Locate every blood parasite and identify its species.
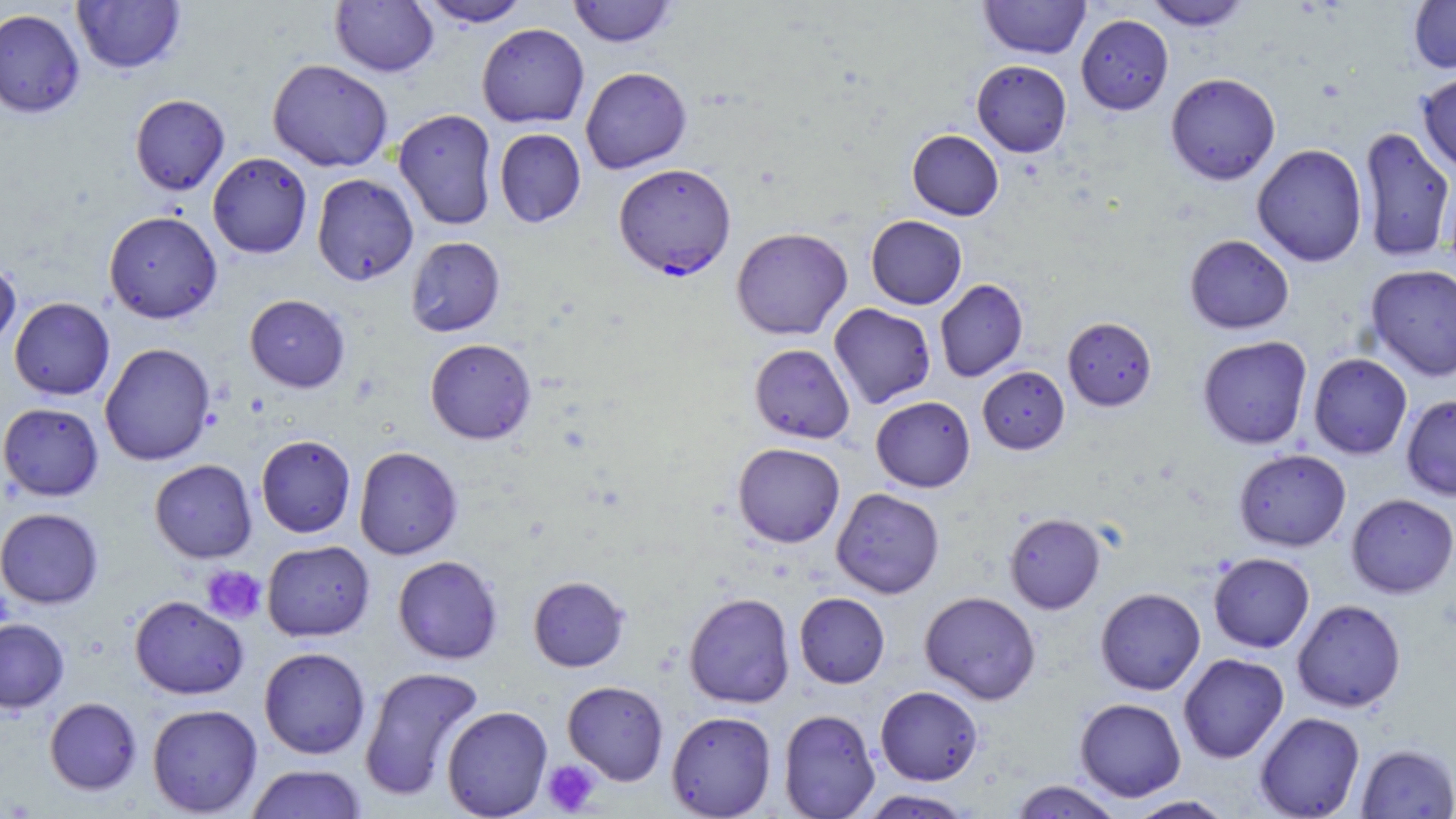

Approximate bounding boxes as [x1, y1, x2, y2] in pixels.
Plasmodium falciparum-infected red blood cells: [613, 164, 737, 280].
No Plasmodium ovale, Plasmodium malariae, Plasmodium vivax, Babesia divergens, or Trypanosoma brucei observed.

Summary:
  - Uninfected red blood cell locations: [71, 0, 186, 74], [330, 0, 438, 77], [417, 0, 532, 27], [567, 0, 678, 47], [979, 0, 1090, 59], [1143, 0, 1253, 31], [1408, 0, 1456, 73], [0, 8, 85, 118], [1076, 14, 1174, 114], [476, 23, 590, 128], [267, 59, 393, 172], [971, 60, 1072, 157], [580, 67, 691, 174], [1417, 71, 1456, 175], [1165, 72, 1281, 185], [130, 94, 230, 195], [393, 109, 498, 231], [1357, 126, 1455, 262], [494, 128, 586, 228], [907, 129, 1004, 220], [1252, 143, 1368, 267], [207, 152, 312, 259], [311, 174, 419, 285], [103, 211, 222, 323], [866, 215, 967, 309], [731, 227, 853, 340], [1184, 234, 1294, 334], [405, 236, 505, 337], [0, 258, 21, 352], [1365, 264, 1456, 381], [935, 279, 1028, 382], [245, 294, 350, 392], [9, 297, 115, 400], [828, 303, 936, 409], [1062, 316, 1157, 411], [1197, 336, 1313, 449], [425, 338, 536, 444], [99, 342, 216, 466], [749, 343, 855, 443], [1308, 353, 1412, 459], [977, 366, 1069, 454], [1401, 394, 1456, 501], [870, 396, 975, 492], [0, 402, 104, 501], [256, 435, 356, 538], [732, 442, 845, 547], [354, 446, 463, 560], [1234, 449, 1351, 551], [149, 459, 257, 563], [831, 488, 945, 598], [1346, 493, 1456, 598], [0, 508, 103, 608], [1004, 512, 1105, 614], [262, 540, 375, 641], [1208, 552, 1315, 653], [392, 555, 503, 664], [528, 576, 629, 672], [1095, 587, 1206, 695], [919, 591, 1041, 705], [683, 592, 795, 708], [794, 592, 889, 688], [129, 595, 249, 700], [1292, 599, 1406, 712], [0, 618, 69, 713], [259, 647, 370, 759], [1178, 653, 1289, 763], [359, 665, 485, 801], [562, 680, 669, 785], [875, 685, 983, 785], [44, 697, 142, 795], [1074, 698, 1186, 802], [147, 703, 262, 817], [441, 705, 553, 818], [778, 708, 880, 818], [666, 710, 776, 818], [1254, 712, 1365, 819], [1356, 743, 1456, 818], [245, 764, 367, 819], [1007, 780, 1127, 818], [858, 789, 975, 818], [1124, 795, 1236, 818]
  - Platelet locations: [200, 565, 266, 623], [541, 759, 600, 816]
  - Slide-level diagnosis: Plasmodium falciparum
  - Magnification: 1000x
  - Stain: May-Grünwald-Giemsa
  - Preparation: thin blood smear
  - Field of view: single
  - Modality: light microscopy
  - Image size: 1456×819 pixels